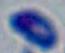
Summary:
  - Magnification: 1000x
  - Modality: micrograph
  - Identification: Toxoplasma gondii